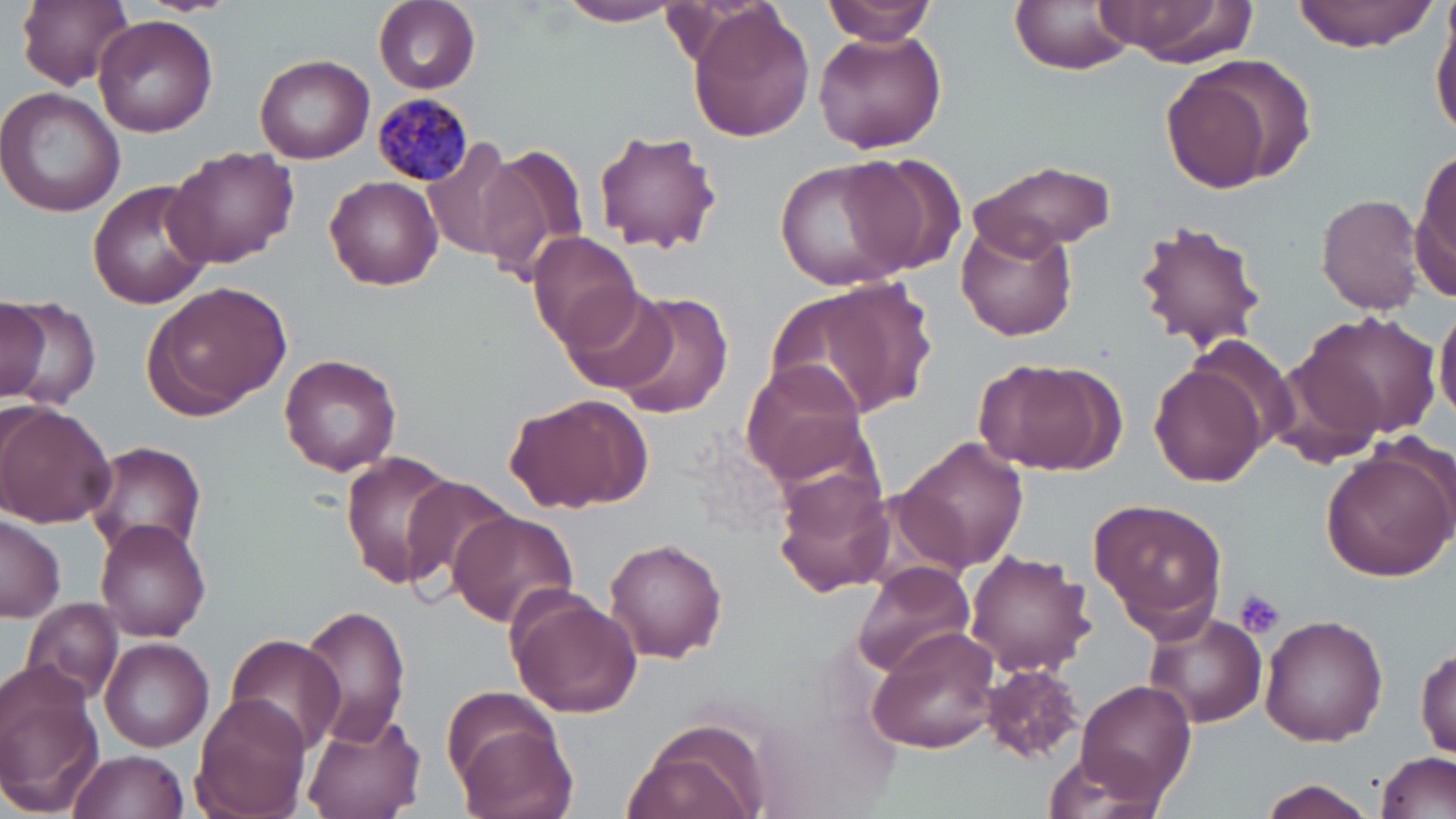

Approximate bounding boxes as (x1, y1, x2, y2) in pixels. Platelet locations: (1233, 587, 1286, 640). Uninfected red blood cell locations: (17, 0, 134, 89), (823, 0, 940, 45), (1009, 0, 1136, 75), (1088, 0, 1258, 64), (1290, 0, 1435, 52), (556, 1, 685, 26), (373, 2, 481, 93), (690, 5, 815, 145), (1430, 7, 1456, 145), (94, 15, 219, 137), (814, 27, 947, 155), (255, 53, 375, 164), (1160, 54, 1315, 191), (0, 87, 128, 219), (592, 129, 726, 253), (423, 138, 526, 259), (164, 144, 298, 269), (475, 144, 591, 285), (1414, 147, 1456, 292), (839, 155, 962, 276), (776, 158, 913, 292), (972, 160, 1115, 255), (325, 174, 444, 290), (89, 177, 217, 309), (1317, 193, 1426, 315), (955, 218, 1077, 341), (1135, 218, 1268, 355), (528, 231, 642, 348), (783, 277, 940, 419), (144, 281, 293, 415), (555, 287, 679, 394), (611, 291, 736, 419), (3, 293, 99, 406), (1, 301, 47, 399), (1435, 302, 1456, 427), (1294, 311, 1439, 442), (279, 352, 402, 475), (971, 354, 1126, 477), (1148, 358, 1269, 486), (739, 360, 871, 484), (505, 392, 649, 513), (0, 403, 118, 530), (897, 435, 1029, 576), (85, 441, 208, 560), (1320, 444, 1456, 580), (338, 451, 467, 588), (771, 468, 895, 598), (397, 480, 517, 599), (1088, 497, 1228, 637), (445, 511, 578, 628), (0, 515, 66, 622), (94, 520, 213, 642), (603, 536, 729, 664), (964, 550, 1096, 678), (854, 561, 974, 676), (506, 593, 642, 718), (20, 595, 127, 709), (300, 604, 412, 748), (1144, 612, 1268, 728), (1259, 613, 1388, 747), (866, 625, 1006, 754), (1098, 629, 1231, 770), (225, 633, 348, 757), (99, 637, 214, 751), (1415, 645, 1455, 760), (979, 663, 1086, 764), (0, 670, 104, 817), (1074, 680, 1196, 807), (442, 686, 562, 785), (192, 693, 310, 819), (300, 712, 426, 819), (621, 717, 771, 819), (454, 721, 577, 819), (67, 748, 191, 819), (1376, 750, 1456, 819), (1037, 755, 1166, 819), (1258, 779, 1378, 818). Plasmodium malariae-infected red blood cell locations: (375, 95, 475, 183). Slide-level diagnosis: Plasmodium malariae. Captured at 1000x magnification. Thin blood film. Optical microscopy. Image is 1456×819 pixels. May-Grünwald-Giemsa-stained preparation. One field of a larger specimen.